Assess for Plasmodium parasites.
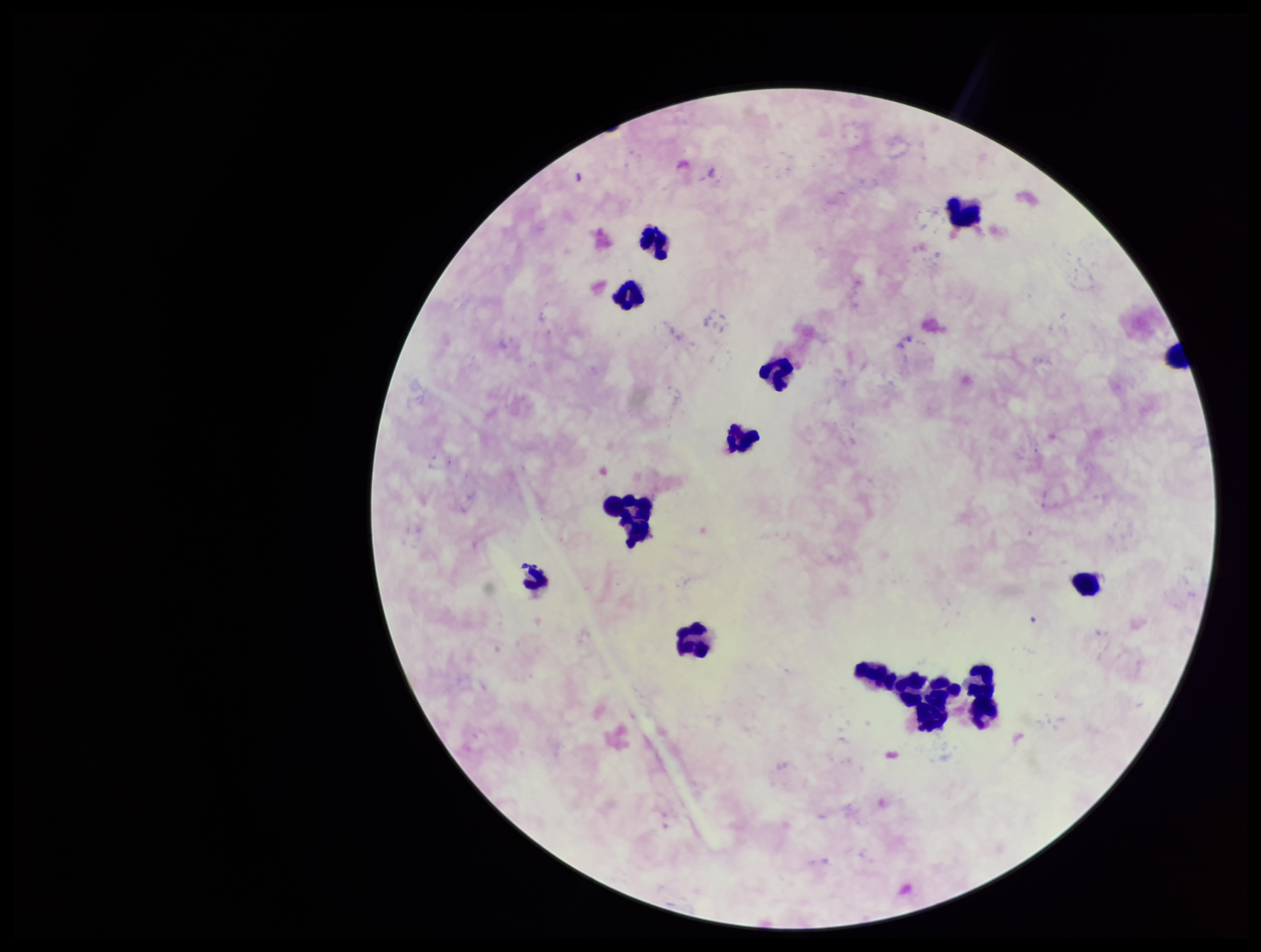
None seen.

Summary:
  - Leukocyte count: 16
  - Patient malaria status: negative
  - Stain: Giemsa
  - Parasite count: 0
  - Field of view: one from this slide
  - Capture: smartphone photograph through the microscope eyepiece
  - Image size: 1261×952 pixels
  - Preparation: thick blood smear